Locate and identify every blood parasite.
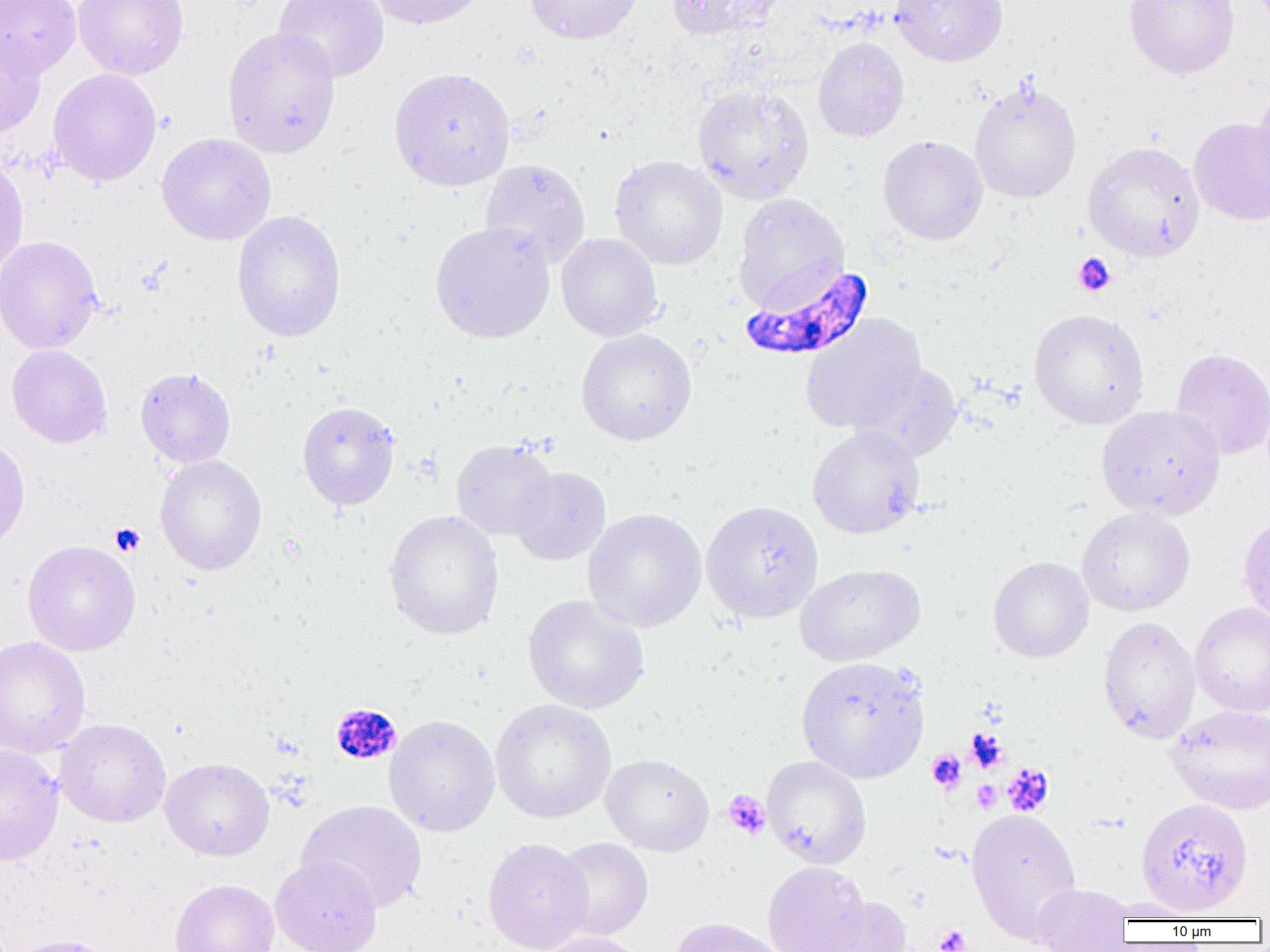
Approximate bounding boxes as (x1,y1)-(x2,y2) corner pairs in pixels.
Plasmodium falciparum-infected red blood cells: (739,260)-(874,361).
No Plasmodium ovale, Plasmodium malariae, Plasmodium vivax, Babesia divergens, or Trypanosoma brucei observed.

Platelet locations: (1073,253)-(1116,297), (110,523)-(145,556), (330,702)-(407,767), (968,731)-(1005,771), (927,750)-(966,792), (1003,764)-(1054,816), (972,781)-(1001,812), (722,790)-(771,840), (934,924)-(970,952). Uninfected red blood cell locations: (0,0)-(81,77), (72,0)-(189,80), (274,0)-(390,82), (366,0)-(488,30), (525,0)-(642,45), (666,0)-(783,41), (890,0)-(1008,66), (1123,0)-(1239,80), (222,25)-(341,159), (0,32)-(46,138), (813,37)-(910,142), (389,67)-(515,191), (48,68)-(162,186), (969,79)-(1081,204), (692,84)-(814,203), (1251,86)-(1270,192), (1189,116)-(1270,226), (156,133)-(276,245), (878,135)-(988,245), (1082,141)-(1205,262), (0,153)-(29,275), (609,155)-(728,270), (479,159)-(590,266), (732,194)-(848,311), (232,210)-(346,342), (429,221)-(555,343), (556,233)-(663,342), (0,235)-(103,354), (1028,308)-(1150,429), (801,315)-(926,434), (575,328)-(697,445), (7,344)-(113,448), (1170,348)-(1270,460), (853,362)-(962,460), (135,366)-(236,468), (297,400)-(400,510), (1096,404)-(1225,520), (807,425)-(926,539), (0,433)-(30,551), (451,439)-(557,540), (155,454)-(267,576), (509,466)-(611,565), (701,500)-(823,623), (1076,507)-(1195,616), (583,508)-(707,633), (383,510)-(504,640), (1237,513)-(1270,625), (22,540)-(141,656), (988,556)-(1093,662), (795,563)-(925,666), (523,594)-(650,715), (1190,601)-(1270,717), (1098,616)-(1201,743), (0,635)-(91,758), (796,656)-(929,783), (490,699)-(616,822), (1167,704)-(1270,814), (384,714)-(501,837), (54,718)-(171,827), (0,743)-(63,866), (601,754)-(714,856), (762,756)-(871,867), (160,757)-(274,861), (1135,797)-(1253,917), (297,800)-(427,913), (966,808)-(1082,942), (483,837)-(594,952), (550,837)-(654,942), (270,856)-(382,952), (762,861)-(870,952), (169,878)-(279,952), (1032,883)-(1133,951), (812,895)-(914,951), (1102,900)-(1206,922), (670,917)-(785,952), (538,932)-(648,952), (5,933)-(118,952). Slide-level diagnosis: Plasmodium falciparum. Image is 1270×952 pixels. Light microscopy. Thin blood film. Captured at 1000x magnification. Single field of view.